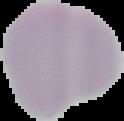 The area outside the segmented cell region is set to black. From a thin blood film. Image is 124×121 pixels. Result: negative for malaria parasites.